Name the cell type shown.
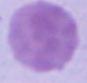

An erythrocyte.

Summary:
  - Modality: photomicrograph
  - Magnification: 1000x